Locate every malaria parasite.
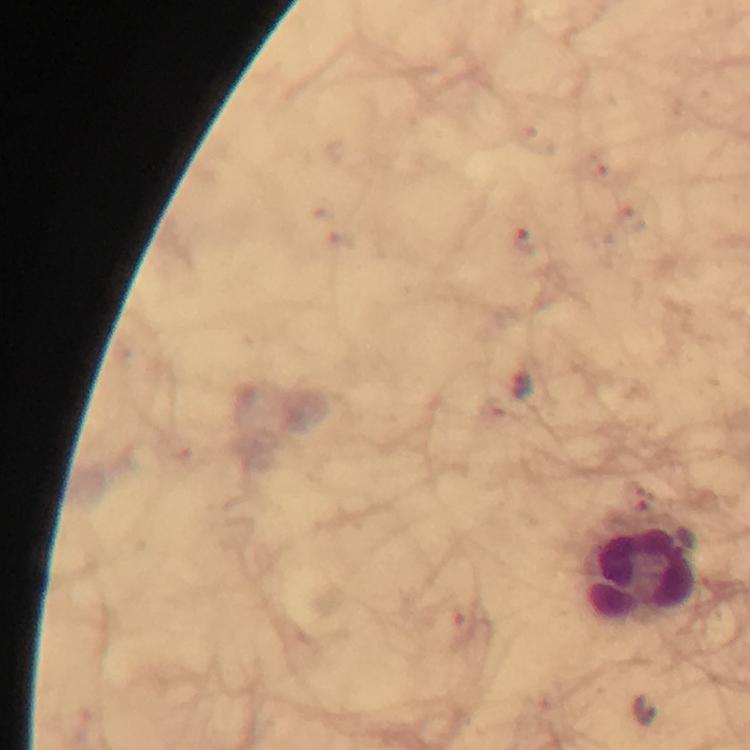

Approximate centers as {x, y} in pixels.
Malaria parasites: {525, 240}, {522, 384}, {465, 627}, {643, 711}.

Leukocyte locations: {643, 575}. Smartphone photograph taken through a microscope. From a malaria diagnostic workup. A crop from one field of view. At 100x magnification. Image is 750×750 pixels. Thick blood smear. Giemsa-stained preparation. Immersion oil applied.